State the blood parasite species.
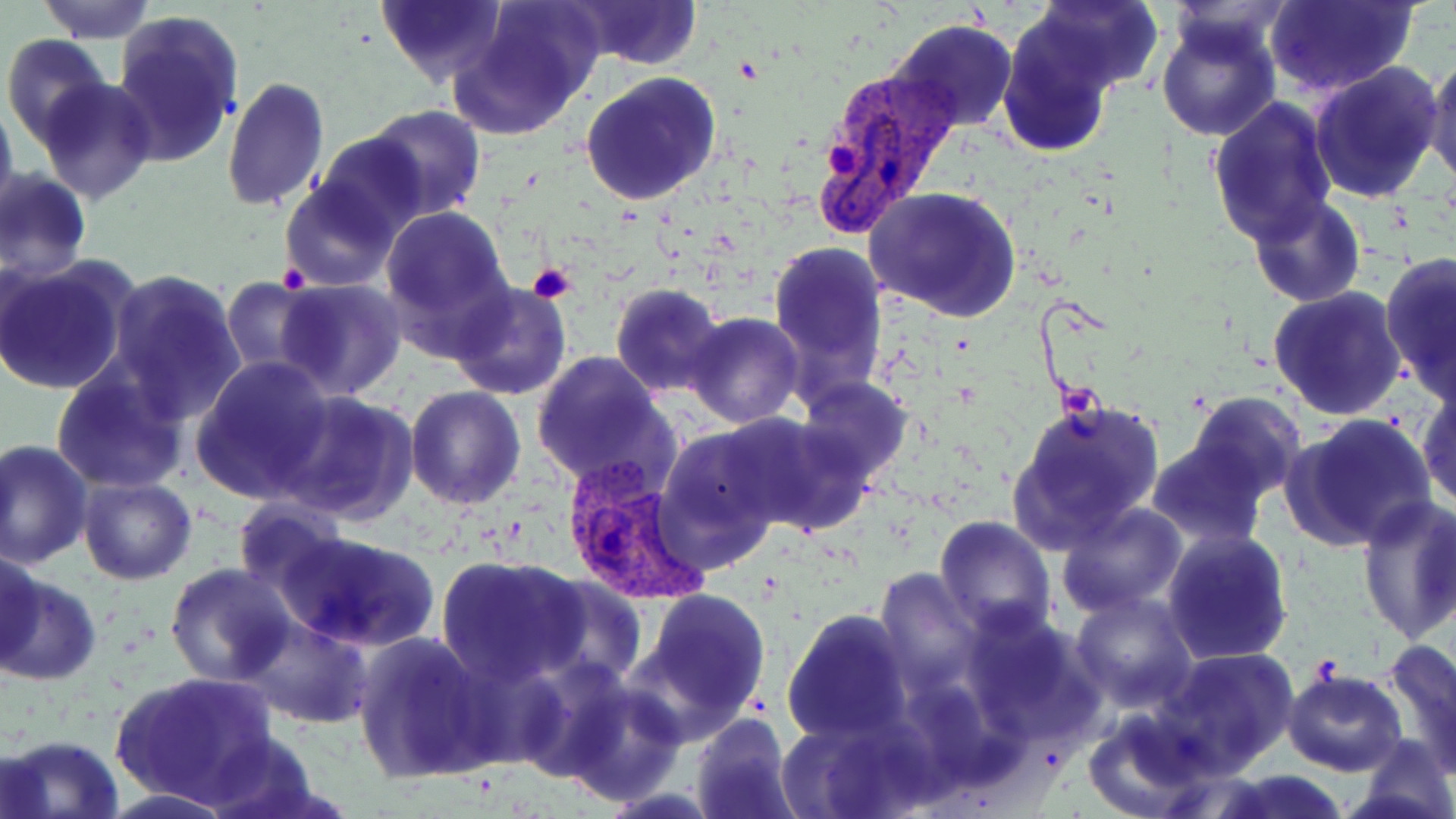
Plasmodium vivax.

Approximate bounding boxes as (x1,y1)-(x2,y2) corner pairs in pixels. Plasmodium vivax-infected red blood cell locations: (809,61)-(964,234), (556,458)-(711,609). Platelet locations: (824,144)-(858,177), (278,261)-(311,292), (527,262)-(576,305). Uninfected red blood cell locations: (377,0)-(507,88), (564,0)-(703,71), (1264,0)-(1417,96), (35,1)-(157,42), (458,1)-(604,134), (1022,1)-(1165,98), (110,13)-(241,169), (1156,17)-(1281,143), (891,20)-(1019,132), (998,27)-(1115,159), (3,35)-(116,152), (1423,56)-(1456,187), (1309,61)-(1444,204), (580,73)-(723,208), (38,76)-(158,203), (221,76)-(330,214), (1207,95)-(1340,247), (0,98)-(18,221), (367,104)-(485,217), (313,131)-(430,240), (1,171)-(92,284), (279,178)-(401,292), (863,186)-(1020,322), (1248,195)-(1365,309), (379,204)-(513,332), (768,239)-(888,396), (1380,251)-(1456,398), (0,256)-(135,398), (106,269)-(247,419), (225,277)-(322,377), (275,279)-(408,402), (448,280)-(574,402), (609,283)-(727,398), (1267,285)-(1408,421), (682,311)-(805,428), (530,352)-(677,493), (191,357)-(335,503), (51,365)-(187,492), (795,377)-(913,482), (1417,385)-(1456,512), (405,387)-(525,511), (273,391)-(416,526), (1184,391)-(1306,502), (1008,395)-(1166,552), (1282,414)-(1438,553), (728,415)-(875,539), (653,428)-(783,562), (1,441)-(93,572), (1146,441)-(1270,549), (78,476)-(196,585), (1355,496)-(1456,646), (232,498)-(346,595), (1056,501)-(1188,617), (934,514)-(1056,638), (276,529)-(440,654), (1161,529)-(1293,666), (2,550)-(49,672), (439,556)-(586,685), (164,563)-(297,686), (535,574)-(646,688), (0,576)-(101,686), (636,589)-(772,729), (1070,591)-(1200,712), (783,609)-(913,744), (241,617)-(374,728), (352,631)-(490,783), (1380,639)-(1456,778), (1158,648)-(1299,774), (1282,669)-(1408,776), (112,671)-(278,806), (560,681)-(685,806), (1082,708)-(1210,814), (690,713)-(797,819), (199,732)-(332,818), (1,733)-(125,819), (1353,734)-(1456,819), (1210,770)-(1354,819). Thin blood film. One field of a larger specimen. May-Grünwald-Giemsa-stained preparation. 1000x magnification. Light microscopy. Image is 1456×819 pixels.